Point out every Plasmodium parasite.
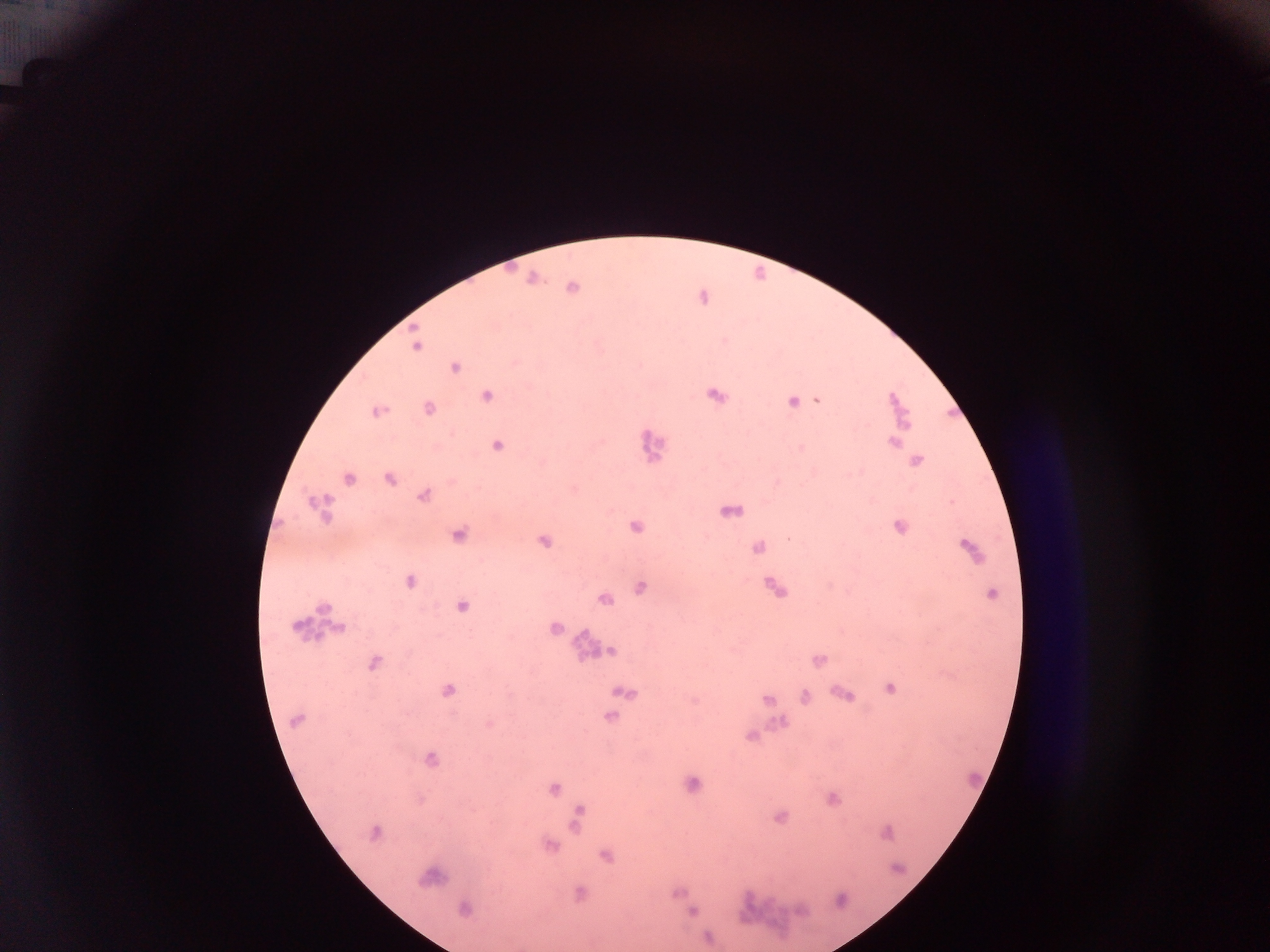
Approximate centers as {x, y} in pixels.
Plasmodium parasites: {531, 281}, {571, 289}, {415, 346}, {454, 368}, {486, 395}, {715, 395}, {816, 399}, {893, 400}, {791, 401}, {429, 407}, {377, 411}, {904, 424}, {892, 441}, {496, 446}, {799, 448}, {915, 461}, {859, 471}, {851, 473}, {389, 479}, {348, 480}, {422, 497}, {310, 502}, {950, 502}, {737, 511}, {728, 512}, {898, 527}, {635, 528}, {458, 534}, {787, 537}, {544, 541}, {967, 546}, {757, 547}, {409, 580}, {640, 587}, {773, 587}, {990, 593}, {605, 599}, {324, 608}, {462, 608}, {298, 628}, {340, 628}, {554, 628}, {612, 650}, {583, 652}, {817, 660}, {374, 662}, {891, 688}, {448, 690}, {623, 692}, {845, 694}, {804, 697}, {767, 699}, {693, 701}, {610, 716}, {780, 720}, {295, 721}, {489, 725}, {750, 736}, {431, 759}, {691, 783}, {554, 788}, {832, 799}, {580, 810}, {779, 817}, {577, 826}, {374, 832}, {885, 832}, {549, 845}, {606, 858}, {428, 877}, {676, 893}, {578, 894}, {463, 908}, {692, 912}, {706, 937}.

country = Ghana
preparation = thick blood smear
field of view = single
image size = 1270×952 pixels
capture = mobile-phone photograph through a microscope